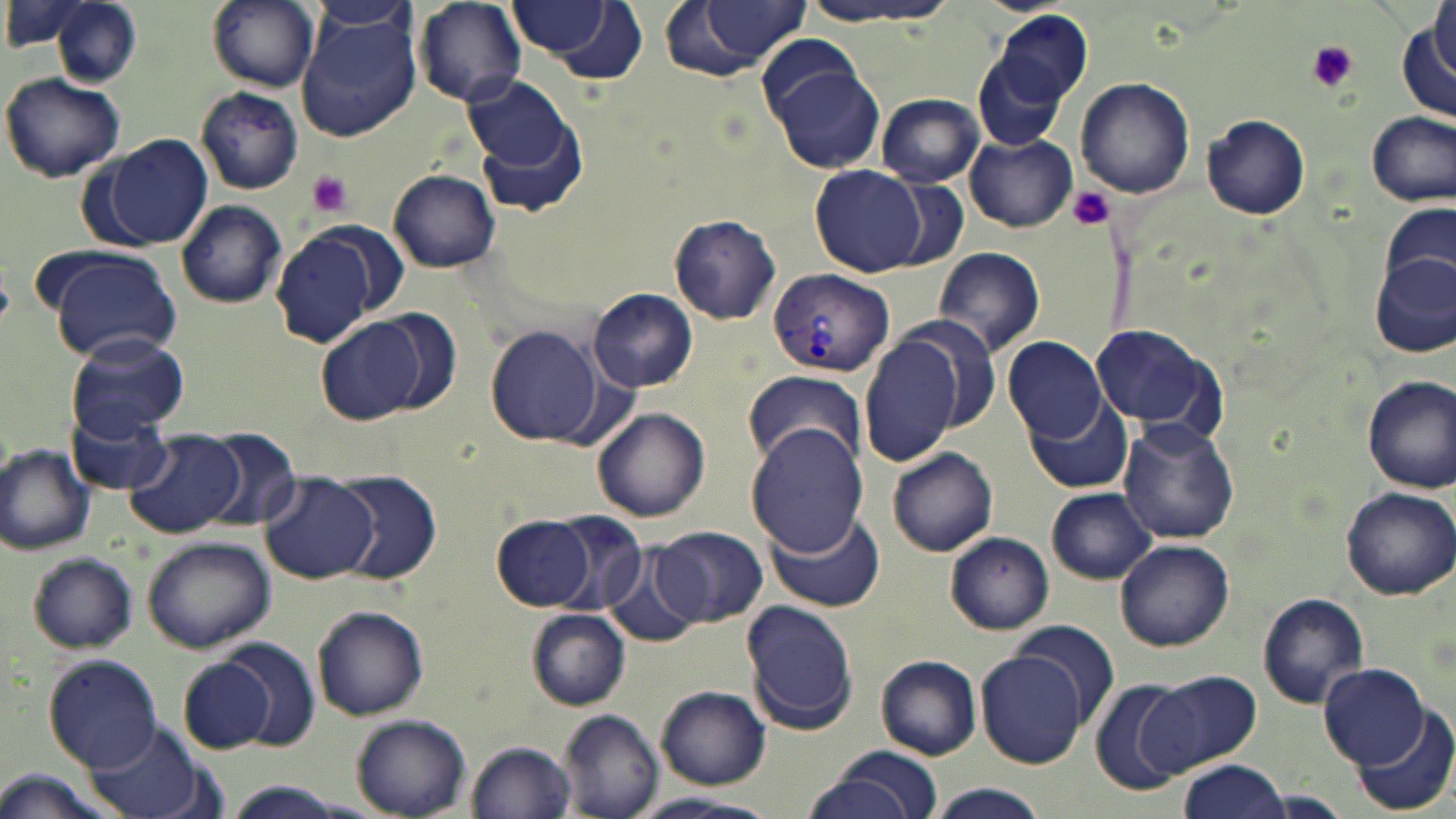

slide-level diagnosis = Plasmodium vivax
modality = light microscopy
Plasmodium vivax-infected red blood cell locations = approximate bounding boxes as named x1/y1/x2/y2 corners in pixels: (x1=767, y1=267, x2=893, y2=376)
magnification = 1000x
platelet locations = approximate bounding boxes as named x1/y1/x2/y2 corners in pixels: (x1=1303, y1=38, x2=1361, y2=95), (x1=306, y1=172, x2=355, y2=219), (x1=1067, y1=185, x2=1115, y2=231)
preparation = thin blood smear
uninfected red blood cell locations = approximate bounding boxes as named x1/y1/x2/y2 corners in pixels: (x1=206, y1=0, x2=319, y2=91), (x1=508, y1=0, x2=648, y2=80), (x1=658, y1=0, x2=808, y2=81), (x1=801, y1=0, x2=957, y2=28), (x1=1430, y1=0, x2=1454, y2=83), (x1=414, y1=1, x2=526, y2=108), (x1=306, y1=2, x2=419, y2=42), (x1=50, y1=4, x2=142, y2=88), (x1=296, y1=9, x2=422, y2=140), (x1=985, y1=9, x2=1092, y2=117), (x1=1395, y1=15, x2=1456, y2=129), (x1=756, y1=34, x2=866, y2=127), (x1=970, y1=47, x2=1072, y2=155), (x1=774, y1=64, x2=886, y2=175), (x1=2, y1=71, x2=126, y2=183), (x1=1076, y1=78, x2=1195, y2=200), (x1=466, y1=79, x2=586, y2=209), (x1=194, y1=86, x2=304, y2=195), (x1=877, y1=94, x2=983, y2=187), (x1=1367, y1=110, x2=1454, y2=207), (x1=1202, y1=114, x2=1310, y2=220), (x1=965, y1=134, x2=1077, y2=232), (x1=94, y1=135, x2=213, y2=250), (x1=811, y1=165, x2=925, y2=276), (x1=387, y1=169, x2=502, y2=273), (x1=176, y1=200, x2=288, y2=308), (x1=1381, y1=202, x2=1455, y2=294), (x1=668, y1=213, x2=781, y2=325), (x1=271, y1=230, x2=383, y2=347), (x1=933, y1=245, x2=1046, y2=356), (x1=43, y1=248, x2=183, y2=361), (x1=1370, y1=251, x2=1456, y2=359), (x1=589, y1=288, x2=698, y2=391), (x1=371, y1=305, x2=460, y2=417), (x1=316, y1=315, x2=428, y2=425), (x1=1090, y1=322, x2=1224, y2=434), (x1=485, y1=326, x2=605, y2=445), (x1=67, y1=334, x2=189, y2=441), (x1=860, y1=335, x2=963, y2=467), (x1=1004, y1=336, x2=1108, y2=442), (x1=741, y1=369, x2=870, y2=471), (x1=1361, y1=375, x2=1456, y2=493), (x1=1027, y1=398, x2=1133, y2=494), (x1=592, y1=407, x2=711, y2=522), (x1=72, y1=409, x2=173, y2=496), (x1=1117, y1=419, x2=1241, y2=544), (x1=746, y1=422, x2=870, y2=558), (x1=127, y1=430, x2=245, y2=538), (x1=200, y1=430, x2=301, y2=532), (x1=0, y1=443, x2=97, y2=555), (x1=888, y1=447, x2=998, y2=556), (x1=330, y1=468, x2=442, y2=584), (x1=260, y1=473, x2=378, y2=584), (x1=1047, y1=486, x2=1156, y2=584), (x1=1338, y1=486, x2=1454, y2=601), (x1=544, y1=511, x2=649, y2=616), (x1=767, y1=512, x2=885, y2=614), (x1=493, y1=515, x2=594, y2=612), (x1=656, y1=525, x2=767, y2=627), (x1=944, y1=532, x2=1054, y2=635), (x1=141, y1=536, x2=277, y2=654), (x1=1115, y1=540, x2=1234, y2=652), (x1=602, y1=546, x2=701, y2=650), (x1=27, y1=552, x2=141, y2=653), (x1=1257, y1=592, x2=1369, y2=709), (x1=740, y1=599, x2=862, y2=734), (x1=311, y1=606, x2=429, y2=720), (x1=526, y1=610, x2=629, y2=709), (x1=1010, y1=622, x2=1120, y2=728), (x1=216, y1=640, x2=321, y2=750), (x1=976, y1=649, x2=1090, y2=768), (x1=43, y1=654, x2=162, y2=769), (x1=876, y1=654, x2=982, y2=760), (x1=176, y1=655, x2=277, y2=754), (x1=1318, y1=661, x2=1431, y2=769), (x1=1150, y1=668, x2=1263, y2=772), (x1=1090, y1=679, x2=1198, y2=796), (x1=656, y1=687, x2=770, y2=788), (x1=1347, y1=709, x2=1455, y2=816), (x1=556, y1=710, x2=663, y2=818), (x1=351, y1=713, x2=471, y2=817), (x1=80, y1=723, x2=213, y2=818), (x1=465, y1=741, x2=576, y2=819), (x1=807, y1=748, x2=943, y2=819), (x1=1177, y1=760, x2=1291, y2=819), (x1=925, y1=782, x2=1052, y2=819), (x1=629, y1=792, x2=782, y2=819)
field of view = one of a larger specimen
stain = May-Grünwald-Giemsa
image size = 1456×819 pixels